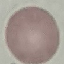 Result: negative for malaria parasites. Thin smear of blood. Giemsa-stained preparation. Automatically extracted cell patch, resized to 64 × 64 pixels. Photographed with a smartphone camera at the microscope eyepiece.